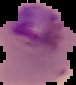
Summary:
  - Result: malaria parasites detected
  - Preparation: thin blood film
  - Image type: cell region segmented out of the field of view; surrounding area masked to black
  - Image size: 76×85 pixels